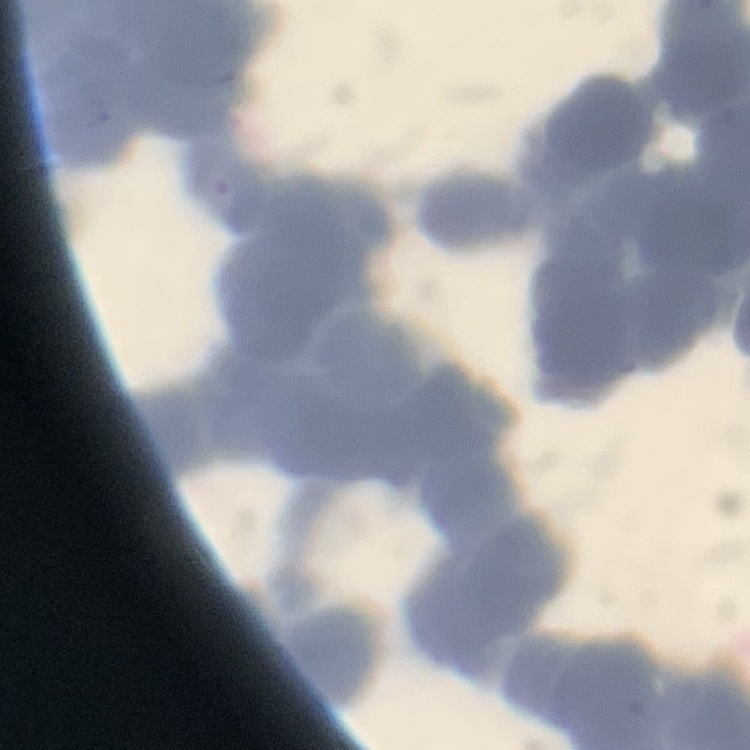 The red blood cells exhibit rouleaux formation. Field's or Giemsa stain. Thin blood smear. One tile cut from a larger photomicrograph.